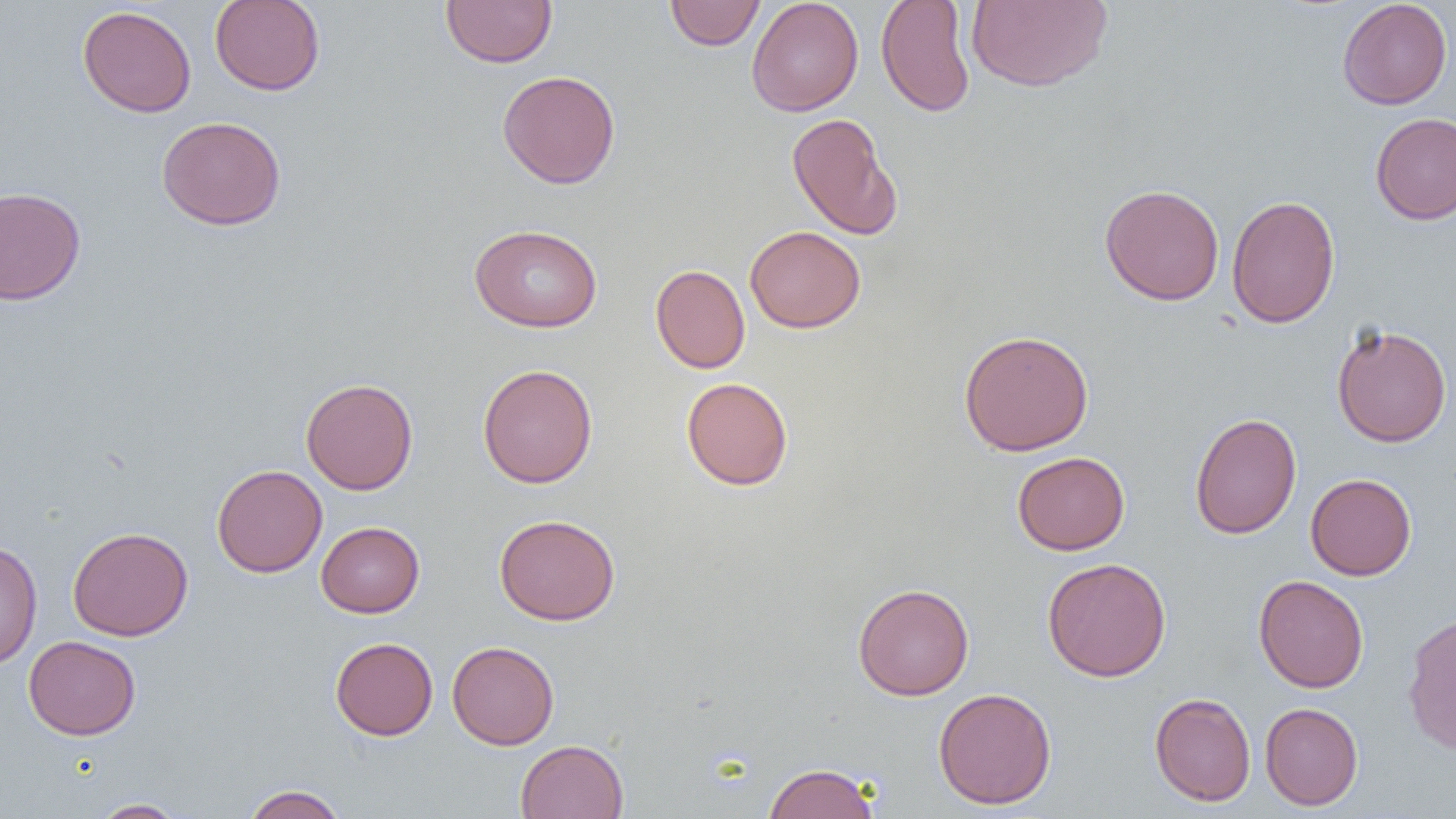

slide-level diagnosis = no evidence of blood parasites
modality = optical microscopy
magnification = 1000x
preparation = thin blood film
uninfected red blood cell locations = approximate bounding boxes as (x1,y1)-(x2,y2) corner pairs in pixels: (210,0)-(326,96), (440,0)-(557,68), (664,0)-(766,50), (746,0)-(864,116), (876,0)-(976,117), (1337,0)-(1453,110), (966,1)-(1112,92), (77,5)-(196,117), (496,70)-(621,189), (786,112)-(902,240), (1370,112)-(1456,225), (157,115)-(286,231), (1099,183)-(1224,306), (0,186)-(86,305), (1226,194)-(1340,329), (470,223)-(603,332), (745,225)-(866,333), (650,264)-(750,373), (1331,323)-(1452,447), (958,329)-(1094,456), (477,363)-(598,488), (301,377)-(418,495), (681,377)-(793,490), (1190,412)-(1302,540), (1012,451)-(1129,555), (212,464)-(327,578), (1305,473)-(1416,580), (494,513)-(621,625), (316,521)-(425,618), (67,526)-(193,641), (0,540)-(42,670), (1042,557)-(1171,682), (1253,574)-(1368,693), (852,583)-(975,700), (1401,611)-(1456,756), (23,635)-(140,740), (330,637)-(438,740), (447,641)-(559,750), (932,687)-(1057,810), (1149,692)-(1256,807), (1259,702)-(1363,810), (515,739)-(629,819), (762,762)-(881,819), (242,784)-(348,819), (90,799)-(187,818)
image size = 1456×819 pixels
field of view = one of a larger specimen